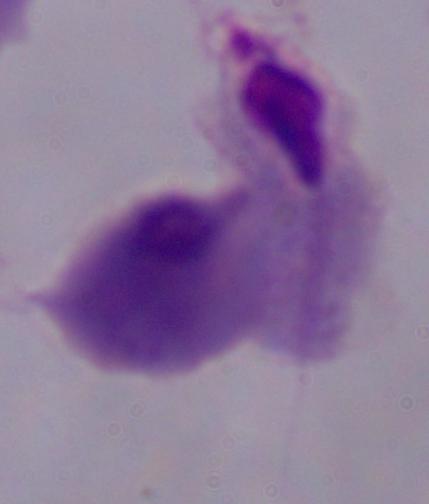
1000x magnification. A trichomonad is seen. Photomicrograph.